Comment on the morphology of the red blood cells.
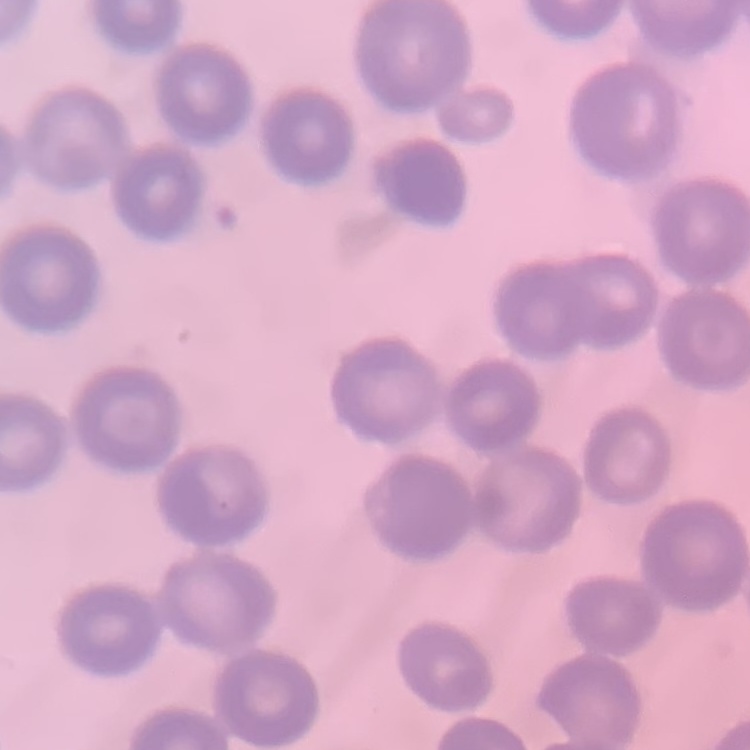

They show no rouleaux formation.

One tile cut from a larger photomicrograph. Thin blood smear. Stained with either Field's or Giemsa.